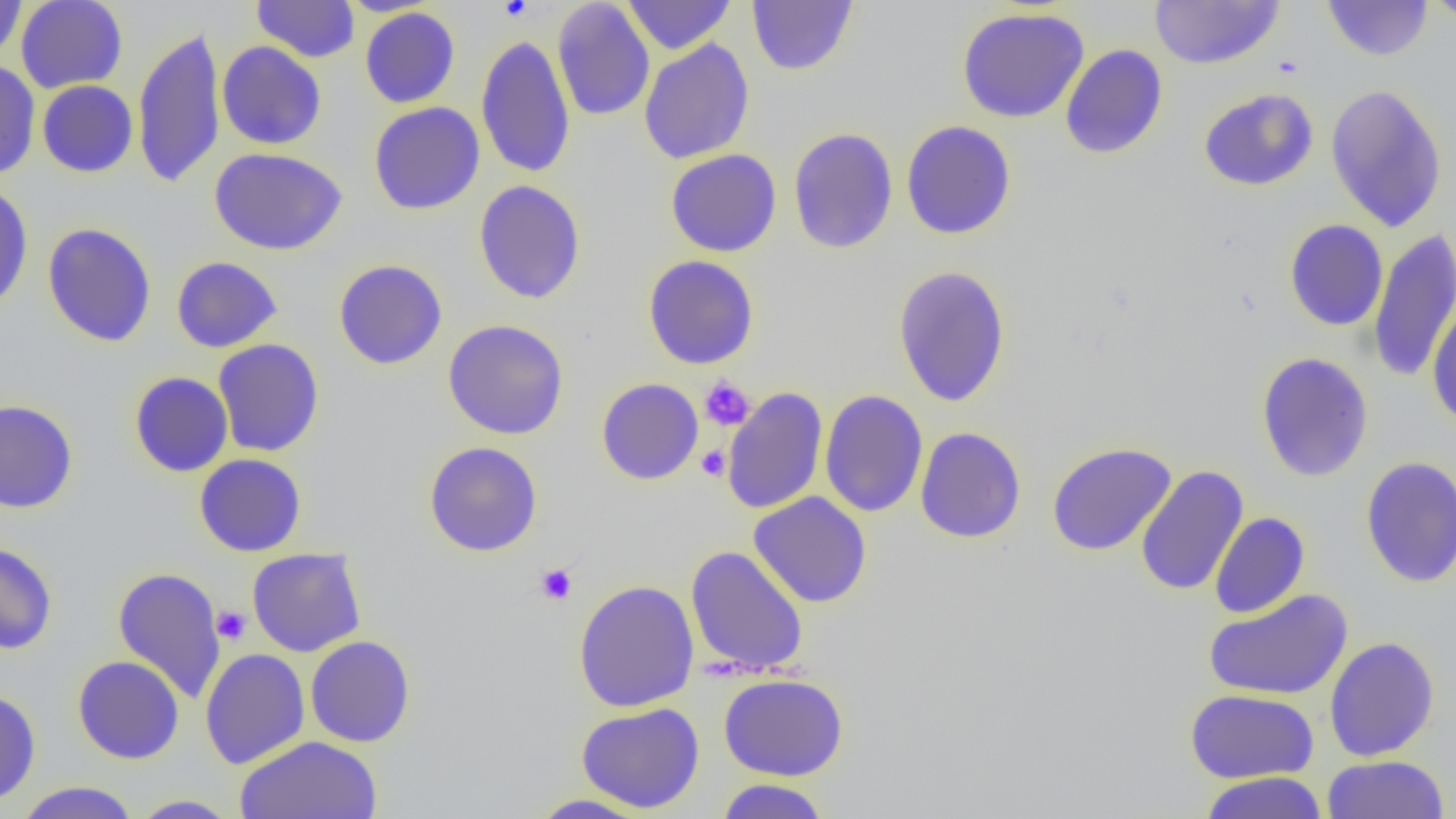

Approximate bounding boxes as [x1, y1, x2, y2] in pixels. Platelet locations: [498, 0, 532, 21], [699, 377, 755, 431], [697, 445, 731, 481], [535, 563, 577, 605], [212, 605, 251, 645]. Uninfected red blood cell locations: [0, 0, 27, 62], [16, 0, 128, 93], [252, 0, 360, 62], [552, 0, 655, 121], [622, 0, 736, 55], [747, 0, 858, 76], [1150, 0, 1285, 69], [1323, 0, 1433, 61], [1423, 0, 1456, 24], [359, 7, 460, 108], [956, 7, 1090, 123], [132, 26, 226, 189], [475, 35, 575, 178], [639, 38, 755, 164], [217, 41, 327, 150], [1060, 44, 1168, 160], [0, 60, 40, 180], [37, 80, 138, 177], [1325, 84, 1448, 232], [1198, 88, 1318, 191], [368, 102, 485, 215], [901, 120, 1016, 240], [787, 127, 898, 255], [209, 147, 347, 255], [665, 149, 782, 257], [474, 180, 586, 304], [0, 183, 33, 315], [1284, 219, 1388, 331], [42, 222, 157, 347], [1367, 228, 1456, 384], [643, 254, 760, 370], [171, 256, 283, 353], [333, 259, 447, 370], [892, 265, 1012, 407], [1426, 300, 1456, 429], [442, 319, 569, 440], [213, 339, 324, 457], [1256, 352, 1373, 482], [129, 371, 234, 477], [596, 378, 704, 485], [721, 386, 828, 515], [819, 390, 928, 517], [0, 399, 78, 514], [915, 427, 1026, 543], [423, 441, 543, 557], [1046, 442, 1177, 557], [194, 453, 306, 557], [1359, 456, 1456, 588], [1135, 465, 1249, 596], [748, 491, 872, 608], [1210, 512, 1310, 619], [0, 541, 58, 654], [685, 545, 809, 678], [247, 548, 366, 657], [112, 566, 226, 703], [573, 579, 699, 712], [1203, 589, 1353, 701], [305, 635, 416, 747], [1324, 636, 1439, 762], [200, 648, 310, 769], [72, 655, 185, 764], [718, 673, 849, 781], [0, 689, 41, 806], [1185, 689, 1319, 784], [576, 703, 705, 813], [235, 735, 383, 818], [1322, 754, 1450, 818], [1198, 771, 1328, 819], [714, 778, 832, 818], [13, 781, 142, 819], [526, 793, 653, 818], [129, 794, 242, 818]. Slide-level diagnosis: no evidence of blood parasites. Image is 1456×819 pixels. Optical microscopy. Thin blood smear. One field of a larger specimen. Captured at 1000x magnification.